Give the position of every Plasmodium parasite.
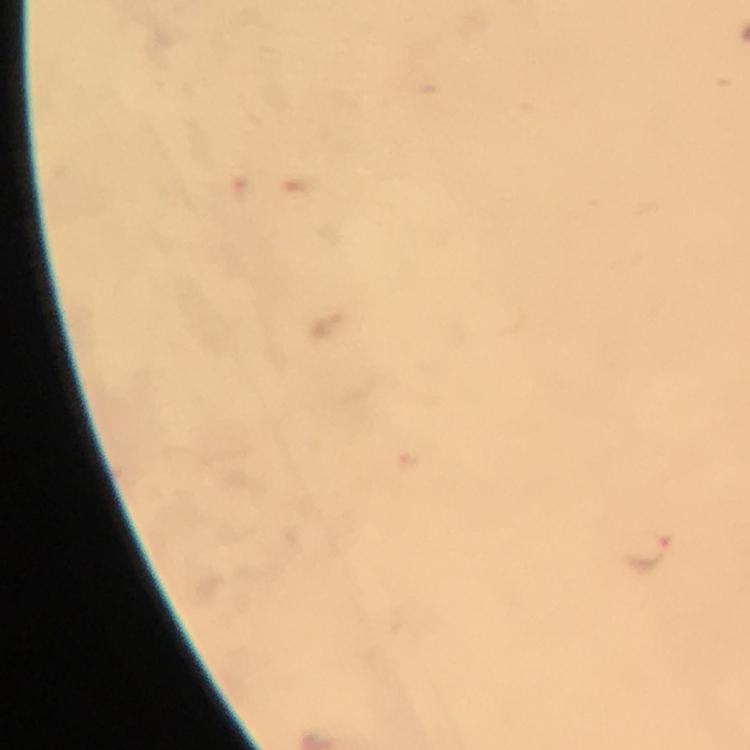

Approximate centers as {x, y} in pixels.
Plasmodium parasites: {647, 551}.

capture = smartphone mounted on the microscope
stain = Giemsa
magnification = 100x
image size = 750×750 pixels
context = from a malaria diagnostic workup
preparation = thick smear
immersion oil = applied
cropped from = a single field of view